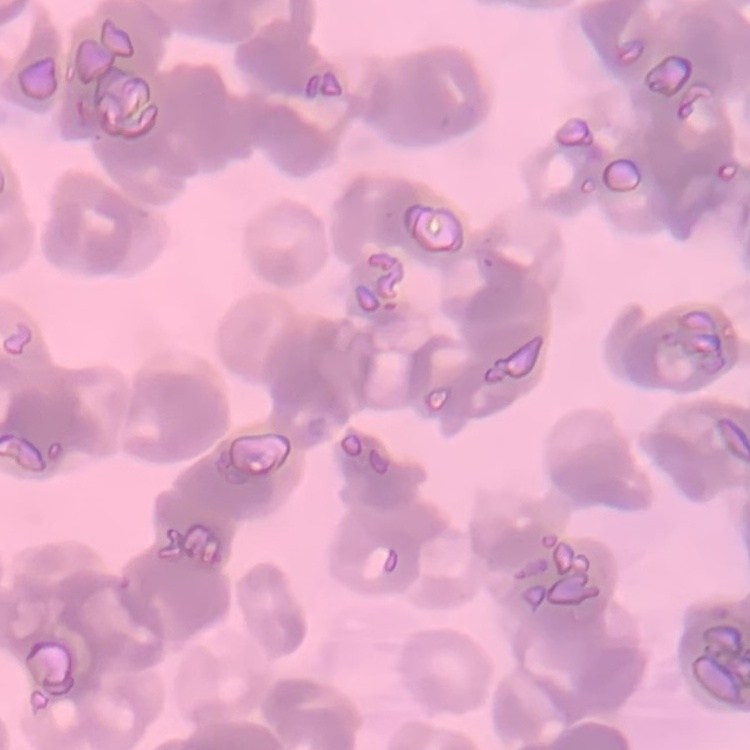

Summary:
  - Erythrocyte morphology: rouleaux formation
  - Preparation: thin blood smear
  - Image type: square crop of a larger photomicrograph
  - Stain: Field's or Giemsa